Classify this cell by malaria status.
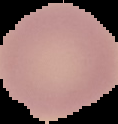

Uninfected.

image size = 118×124 pixels
image type = segmented cell region with the area outside set to black
preparation = thin blood smear